Identify the blood parasite species.
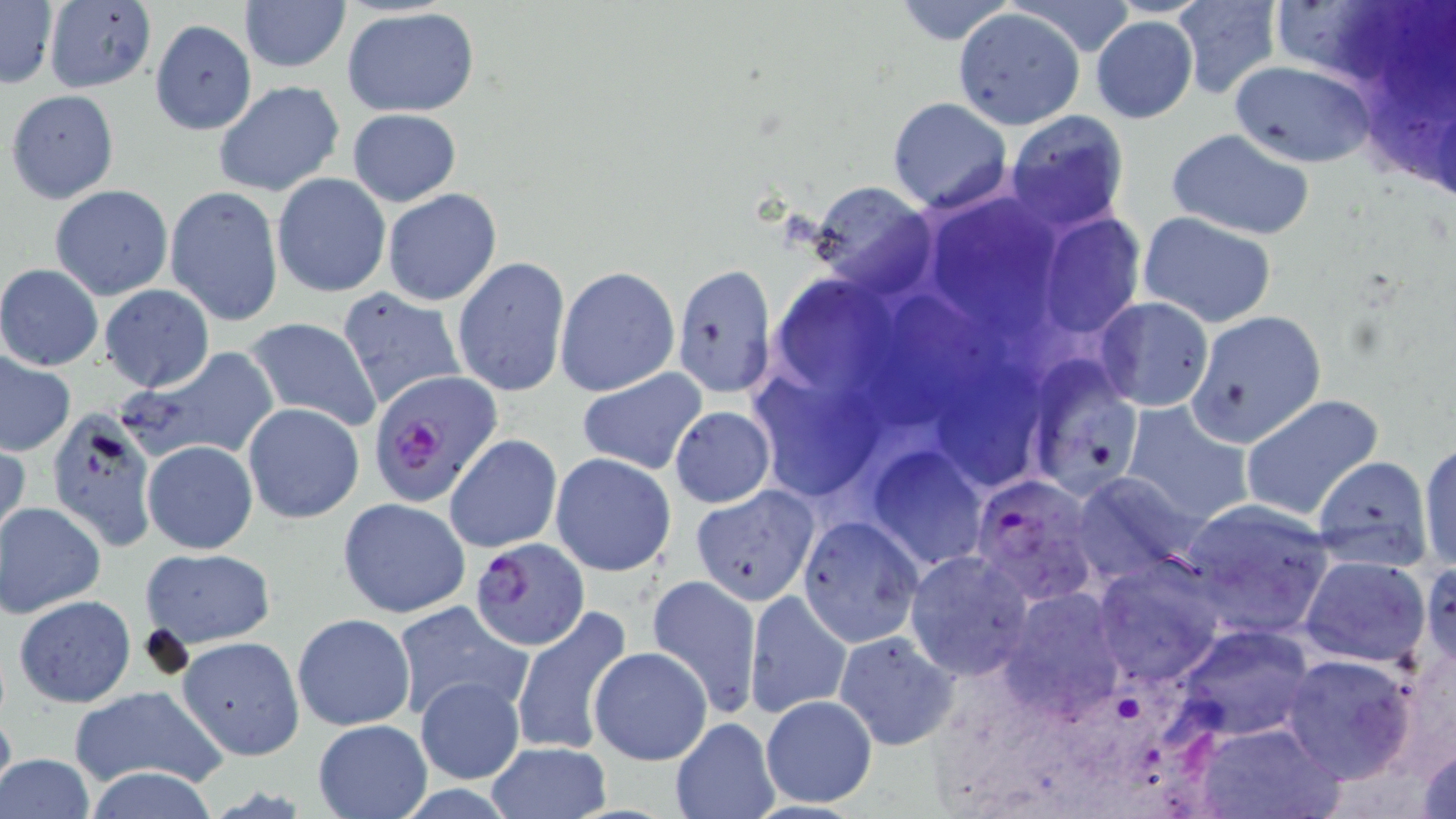

Plasmodium falciparum.

image size = 1456×819 pixels
uninfected red blood cell locations = approximate bounding boxes as (x1, y1, x2, y2) in pixels: (0, 0, 58, 90), (238, 0, 351, 74), (889, 0, 1021, 46), (1171, 0, 1283, 99), (42, 1, 158, 94), (340, 7, 481, 115), (953, 7, 1085, 130), (1092, 15, 1199, 123), (150, 19, 256, 135), (1228, 60, 1378, 167), (213, 80, 345, 197), (6, 89, 119, 204), (888, 97, 1013, 213), (348, 108, 461, 207), (1004, 110, 1128, 233), (1166, 126, 1318, 240), (272, 173, 392, 298), (806, 180, 937, 295), (50, 185, 174, 300), (165, 185, 286, 327), (383, 188, 502, 306), (934, 210, 1075, 343), (1041, 212, 1142, 336), (1137, 212, 1279, 328), (453, 256, 570, 398), (0, 263, 104, 371), (554, 265, 680, 397), (673, 265, 778, 395), (98, 284, 215, 392), (778, 285, 905, 393), (335, 286, 467, 412), (879, 289, 1015, 436), (1094, 298, 1214, 412), (1186, 309, 1327, 449), (244, 317, 383, 431), (116, 347, 283, 469), (0, 351, 77, 456), (1023, 359, 1145, 501), (576, 368, 709, 476), (953, 369, 1058, 500), (751, 375, 887, 499), (1240, 393, 1386, 522), (1119, 399, 1253, 527), (242, 403, 364, 523), (669, 405, 776, 509), (45, 406, 160, 551), (444, 434, 562, 553), (0, 435, 29, 552), (141, 439, 258, 555), (1419, 440, 1456, 575), (865, 446, 991, 573), (550, 452, 677, 576), (1314, 454, 1433, 570), (1068, 472, 1201, 583), (689, 484, 820, 607), (338, 496, 471, 619), (1178, 499, 1336, 639), (1, 502, 105, 618), (797, 515, 924, 647), (139, 547, 276, 649), (905, 550, 1035, 681), (1092, 556, 1226, 688), (1299, 556, 1432, 668), (1420, 559, 1456, 674), (646, 575, 763, 718), (998, 588, 1130, 720), (745, 590, 852, 719), (13, 594, 136, 707), (392, 602, 530, 721), (513, 607, 636, 758), (292, 612, 417, 731), (1171, 624, 1318, 743), (833, 630, 963, 750), (177, 636, 305, 761), (588, 646, 713, 765), (1280, 652, 1418, 784), (414, 676, 525, 784), (69, 684, 228, 793), (760, 694, 878, 809), (0, 701, 15, 807), (668, 717, 778, 819), (313, 718, 431, 818), (1191, 720, 1341, 819), (1414, 741, 1456, 819), (486, 742, 612, 816), (0, 753, 96, 819), (81, 766, 223, 819)
field of view = single
preparation = thin blood smear
modality = optical microscopy
Plasmodium falciparum-infected red blood cell locations = approximate bounding boxes as (x1, y1, x2, y2) in pixels: (368, 370, 500, 507), (971, 475, 1102, 605), (469, 538, 591, 651)
magnification = 1000x
stain = May-Grünwald-Giemsa